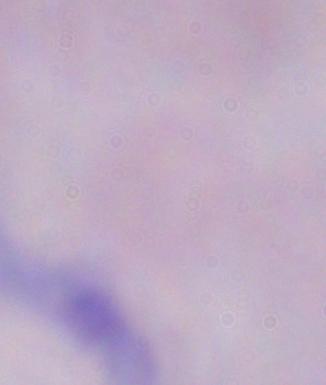

Photomicrograph. A trypanosome is seen. Captured at 1000x magnification.